Report the malaria status of this cell.
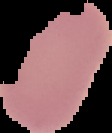
Uninfected.

{
  "image_size": "112×133 pixels",
  "preparation": "thin blood smear",
  "image_type": "segmented cell region on a black background"
}